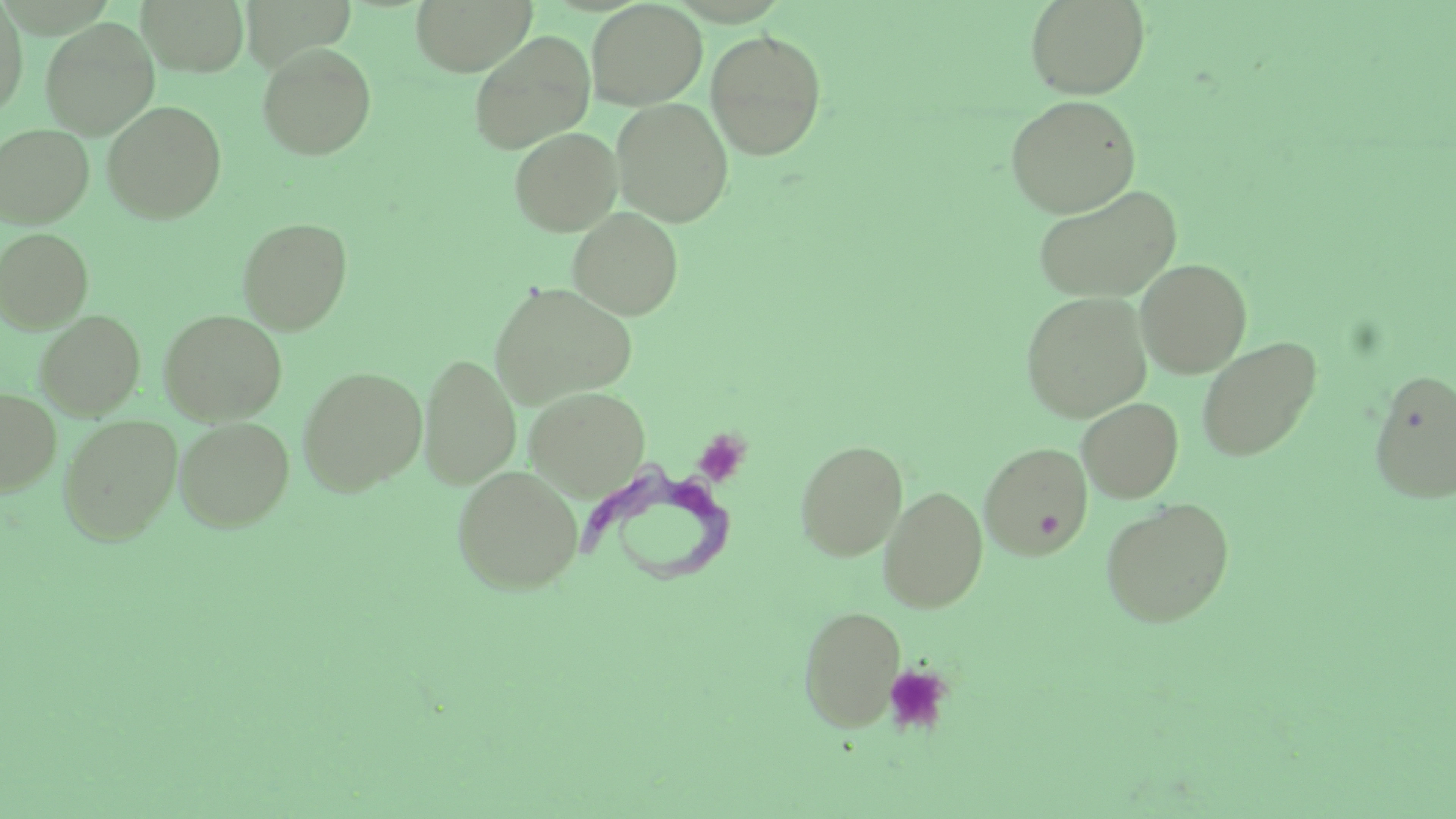

Approximate bounding boxes as (x1,y1)-(x2,y2) corner pairs in pixels. Platelet locations: (692,429)-(751,487), (883,664)-(953,736). Trypanosoma brucei locations: (584,460)-(737,589). Uninfected red blood cell locations: (0,0)-(28,117), (137,0)-(249,76), (411,0)-(536,76), (586,0)-(708,109), (1024,0)-(1150,99), (41,17)-(159,138), (705,29)-(828,160), (468,30)-(595,154), (257,42)-(377,160), (1005,95)-(1142,217), (611,98)-(734,227), (102,100)-(227,224), (0,123)-(95,229), (509,127)-(622,235), (1032,183)-(1184,303), (567,207)-(684,320), (237,217)-(353,335), (0,228)-(93,332), (1135,258)-(1252,378), (489,281)-(638,410), (1020,291)-(1152,423), (159,309)-(287,424), (35,311)-(145,419), (1196,336)-(1322,462), (419,354)-(520,489), (297,366)-(427,495), (1368,367)-(1456,505), (525,386)-(651,500), (0,388)-(61,496), (1077,398)-(1184,502), (58,414)-(183,545), (174,417)-(294,531), (796,439)-(908,560), (979,441)-(1093,559), (452,465)-(584,595), (879,485)-(988,613), (1100,497)-(1235,628), (799,604)-(905,730). Slide-level diagnosis: Trypanosoma brucei. Captured at 1000x magnification. One field of a larger specimen. Optical microscopy. Image is 1456×819 pixels. Thin blood smear. May-Grünwald-Giemsa stain.